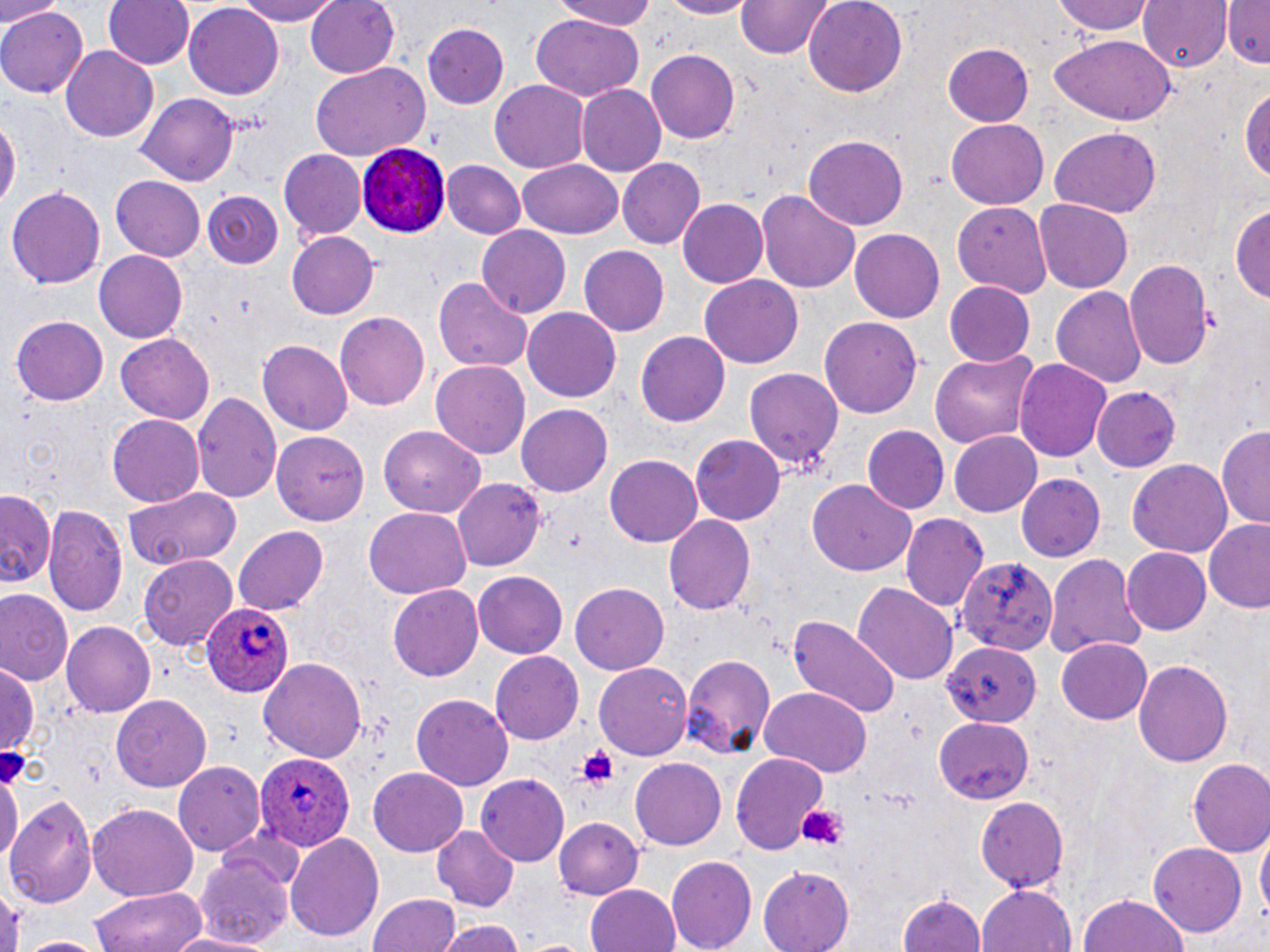

{
  "slide_level_diagnosis": "Plasmodium ovale",
  "stain": "May-Grünwald-Giemsa",
  "field_of_view": "single",
  "uninfected_red_blood_cell_locations": "approximate bounding boxes as named x1/y1/x2/y2 corners in pixels: (x1=0, y1=0, x2=58, y2=26), (x1=104, y1=0, x2=195, y2=71), (x1=227, y1=0, x2=345, y2=25), (x1=306, y1=0, x2=401, y2=79), (x1=551, y1=0, x2=668, y2=29), (x1=654, y1=0, x2=761, y2=18), (x1=802, y1=0, x2=909, y2=97), (x1=1056, y1=0, x2=1156, y2=39), (x1=1140, y1=0, x2=1229, y2=73), (x1=1224, y1=0, x2=1270, y2=68), (x1=735, y1=1, x2=834, y2=59), (x1=184, y1=4, x2=283, y2=100), (x1=0, y1=5, x2=87, y2=98), (x1=529, y1=15, x2=645, y2=100), (x1=423, y1=23, x2=508, y2=107), (x1=1051, y1=36, x2=1176, y2=124), (x1=943, y1=43, x2=1035, y2=126), (x1=62, y1=47, x2=159, y2=143), (x1=645, y1=47, x2=740, y2=142), (x1=310, y1=63, x2=430, y2=162), (x1=488, y1=80, x2=589, y2=175), (x1=1239, y1=82, x2=1270, y2=191), (x1=578, y1=85, x2=666, y2=175), (x1=137, y1=94, x2=241, y2=185), (x1=0, y1=113, x2=19, y2=215), (x1=947, y1=120, x2=1048, y2=208), (x1=1049, y1=128, x2=1162, y2=217), (x1=800, y1=135, x2=909, y2=230), (x1=279, y1=149, x2=366, y2=240), (x1=517, y1=158, x2=624, y2=241), (x1=616, y1=158, x2=706, y2=251), (x1=442, y1=160, x2=526, y2=238), (x1=109, y1=175, x2=208, y2=261), (x1=7, y1=183, x2=105, y2=286), (x1=204, y1=190, x2=284, y2=268), (x1=758, y1=190, x2=860, y2=295), (x1=678, y1=198, x2=768, y2=287), (x1=1033, y1=199, x2=1133, y2=294), (x1=1229, y1=201, x2=1270, y2=304), (x1=954, y1=203, x2=1054, y2=297), (x1=476, y1=225, x2=571, y2=317), (x1=850, y1=227, x2=945, y2=322), (x1=287, y1=230, x2=379, y2=319), (x1=580, y1=246, x2=670, y2=334), (x1=93, y1=250, x2=187, y2=342), (x1=1124, y1=259, x2=1213, y2=374), (x1=701, y1=276, x2=803, y2=367), (x1=435, y1=277, x2=531, y2=375), (x1=944, y1=281, x2=1036, y2=367), (x1=1050, y1=285, x2=1148, y2=390), (x1=523, y1=307, x2=622, y2=402), (x1=335, y1=312, x2=431, y2=410), (x1=10, y1=315, x2=108, y2=405), (x1=819, y1=317, x2=924, y2=419), (x1=636, y1=331, x2=732, y2=427), (x1=114, y1=332, x2=216, y2=424), (x1=259, y1=340, x2=352, y2=434), (x1=928, y1=350, x2=1041, y2=450), (x1=1014, y1=357, x2=1113, y2=463), (x1=431, y1=360, x2=530, y2=460), (x1=740, y1=367, x2=841, y2=477), (x1=1090, y1=386, x2=1180, y2=473), (x1=193, y1=392, x2=281, y2=505), (x1=517, y1=404, x2=613, y2=496), (x1=106, y1=416, x2=204, y2=506), (x1=863, y1=425, x2=950, y2=515), (x1=381, y1=426, x2=487, y2=515), (x1=1217, y1=426, x2=1270, y2=528), (x1=272, y1=429, x2=371, y2=524), (x1=947, y1=431, x2=1041, y2=518), (x1=691, y1=434, x2=785, y2=525), (x1=605, y1=456, x2=704, y2=547), (x1=1126, y1=459, x2=1233, y2=557), (x1=1015, y1=473, x2=1105, y2=562), (x1=451, y1=477, x2=547, y2=571), (x1=806, y1=479, x2=916, y2=576), (x1=120, y1=486, x2=242, y2=569), (x1=0, y1=487, x2=56, y2=591), (x1=45, y1=503, x2=130, y2=621), (x1=362, y1=507, x2=471, y2=598), (x1=899, y1=511, x2=989, y2=613), (x1=663, y1=514, x2=754, y2=617), (x1=1204, y1=521, x2=1270, y2=613), (x1=232, y1=526, x2=329, y2=615), (x1=1122, y1=547, x2=1212, y2=635), (x1=138, y1=554, x2=240, y2=650), (x1=959, y1=554, x2=1059, y2=654), (x1=1046, y1=554, x2=1146, y2=659), (x1=473, y1=572, x2=566, y2=657), (x1=388, y1=582, x2=484, y2=678), (x1=571, y1=582, x2=671, y2=674), (x1=853, y1=582, x2=959, y2=685), (x1=1, y1=588, x2=74, y2=687), (x1=787, y1=616, x2=902, y2=720), (x1=62, y1=623, x2=154, y2=717), (x1=1057, y1=637, x2=1152, y2=722), (x1=942, y1=640, x2=1040, y2=727), (x1=489, y1=650, x2=584, y2=743), (x1=681, y1=652, x2=775, y2=761), (x1=261, y1=657, x2=368, y2=768), (x1=1132, y1=658, x2=1233, y2=769), (x1=1, y1=661, x2=39, y2=764), (x1=594, y1=662, x2=690, y2=759), (x1=758, y1=687, x2=873, y2=775), (x1=110, y1=694, x2=213, y2=791), (x1=411, y1=695, x2=512, y2=789), (x1=934, y1=717, x2=1034, y2=804), (x1=730, y1=752, x2=830, y2=855), (x1=629, y1=758, x2=725, y2=850), (x1=1188, y1=758, x2=1270, y2=857), (x1=0, y1=761, x2=21, y2=878), (x1=173, y1=762, x2=264, y2=859), (x1=366, y1=767, x2=469, y2=857), (x1=475, y1=773, x2=570, y2=863), (x1=6, y1=795, x2=98, y2=908), (x1=975, y1=796, x2=1070, y2=891), (x1=88, y1=804, x2=199, y2=901), (x1=554, y1=817, x2=642, y2=900), (x1=431, y1=825, x2=519, y2=912), (x1=285, y1=833, x2=385, y2=942), (x1=1256, y1=833, x2=1269, y2=927), (x1=1150, y1=842, x2=1246, y2=935), (x1=194, y1=852, x2=294, y2=950), (x1=665, y1=856, x2=754, y2=952), (x1=757, y1=868, x2=854, y2=952), (x1=585, y1=883, x2=682, y2=952), (x1=978, y1=884, x2=1075, y2=952), (x1=91, y1=885, x2=207, y2=951), (x1=367, y1=890, x2=464, y2=952), (x1=899, y1=891, x2=984, y2=952), (x1=1077, y1=892, x2=1191, y2=952), (x1=434, y1=918, x2=526, y2=952), (x1=160, y1=932, x2=266, y2=952), (x1=16, y1=937, x2=106, y2=952)",
  "plasmodium_ovale_infected_red_blood_cell_locations": "approximate bounding boxes as named x1/y1/x2/y2 corners in pixels: (x1=356, y1=144, x2=451, y2=238), (x1=201, y1=599, x2=292, y2=697), (x1=259, y1=750, x2=356, y2=850)",
  "preparation": "thin blood film",
  "image_size": "1270×952 pixels",
  "magnification": "1000x",
  "platelet_locations": "approximate bounding boxes as named x1/y1/x2/y2 corners in pixels: (x1=572, y1=746, x2=622, y2=789), (x1=798, y1=802, x2=848, y2=851)",
  "modality": "optical microscopy"
}